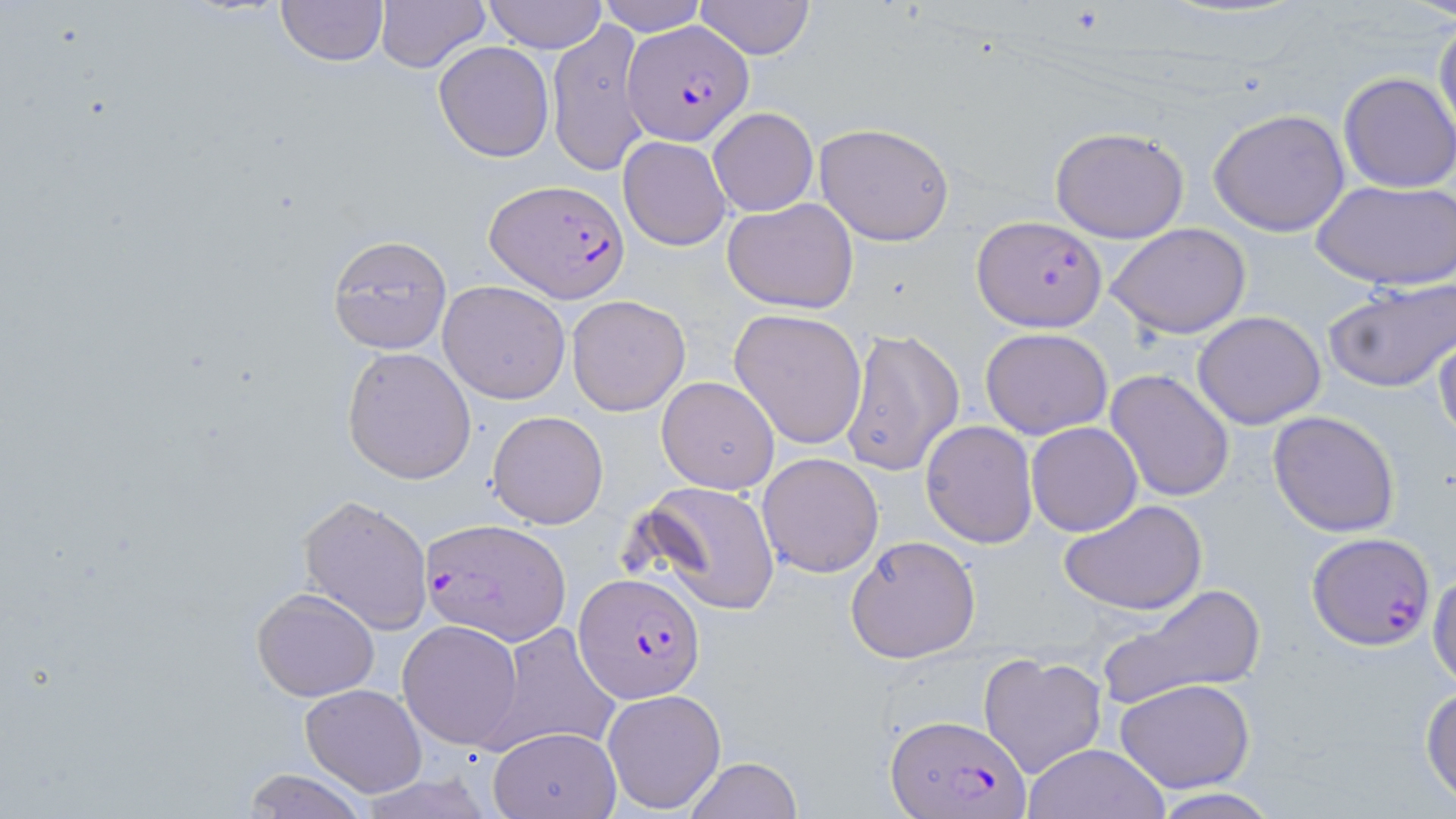
Approximate bounding boxes as [x1, y1, x2, y2] in pixels. Uninfected red blood cell locations: [275, 0, 389, 68], [373, 0, 491, 73], [483, 0, 607, 52], [600, 1, 706, 35], [691, 1, 816, 59], [1434, 15, 1456, 146], [546, 18, 651, 176], [433, 41, 555, 162], [1338, 73, 1456, 192], [708, 107, 818, 217], [1208, 108, 1351, 236], [813, 122, 955, 246], [1048, 126, 1190, 243], [618, 135, 732, 250], [1311, 179, 1455, 289], [722, 196, 859, 314], [1108, 222, 1252, 339], [326, 235, 454, 355], [1322, 277, 1456, 396], [439, 280, 571, 404], [566, 295, 691, 415], [730, 309, 870, 449], [1192, 310, 1326, 429], [1434, 324, 1456, 445], [841, 327, 966, 479], [980, 327, 1114, 440], [342, 346, 477, 485], [1106, 369, 1235, 504], [656, 375, 781, 493], [487, 410, 608, 529], [1269, 410, 1401, 536], [920, 421, 1037, 548], [1026, 421, 1142, 537], [758, 452, 884, 577], [632, 480, 783, 615], [298, 494, 435, 633], [1060, 497, 1209, 616], [845, 535, 983, 664], [1428, 564, 1456, 690], [1095, 584, 1267, 712], [250, 587, 380, 700], [397, 620, 526, 749], [490, 624, 619, 754], [978, 652, 1108, 779], [1114, 679, 1255, 793], [301, 683, 427, 798], [1420, 685, 1456, 804], [602, 689, 726, 811], [487, 726, 621, 818], [1022, 742, 1170, 819], [684, 756, 801, 819], [240, 769, 373, 819], [1144, 787, 1286, 818]. Plasmodium falciparum-infected red blood cell locations: [627, 21, 753, 145], [486, 181, 630, 301], [972, 215, 1108, 331], [420, 516, 570, 645], [1305, 532, 1436, 650], [573, 573, 706, 704], [886, 712, 1027, 819]. Slide-level diagnosis: Plasmodium falciparum. Image is 1456×819 pixels. Thin blood film. Single field of view. May-Grünwald-Giemsa-stained preparation. Light microscopy. Captured at 1000x magnification.